Name the parasite shown.
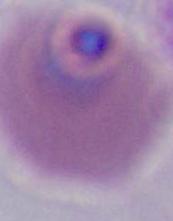
This is Plasmodium.

Summary:
  - Modality: micrograph
  - Magnification: 400x or 1000x